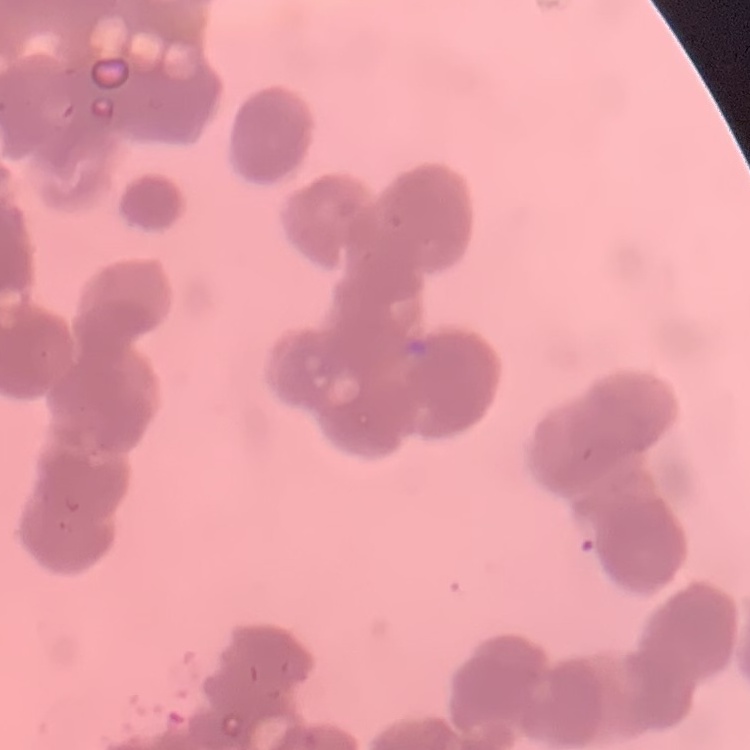
erythrocyte morphology = rouleaux formation
stain = Field's or Giemsa
preparation = thin blood film
image type = one tile cut from a larger photomicrograph